Give the preparation type.
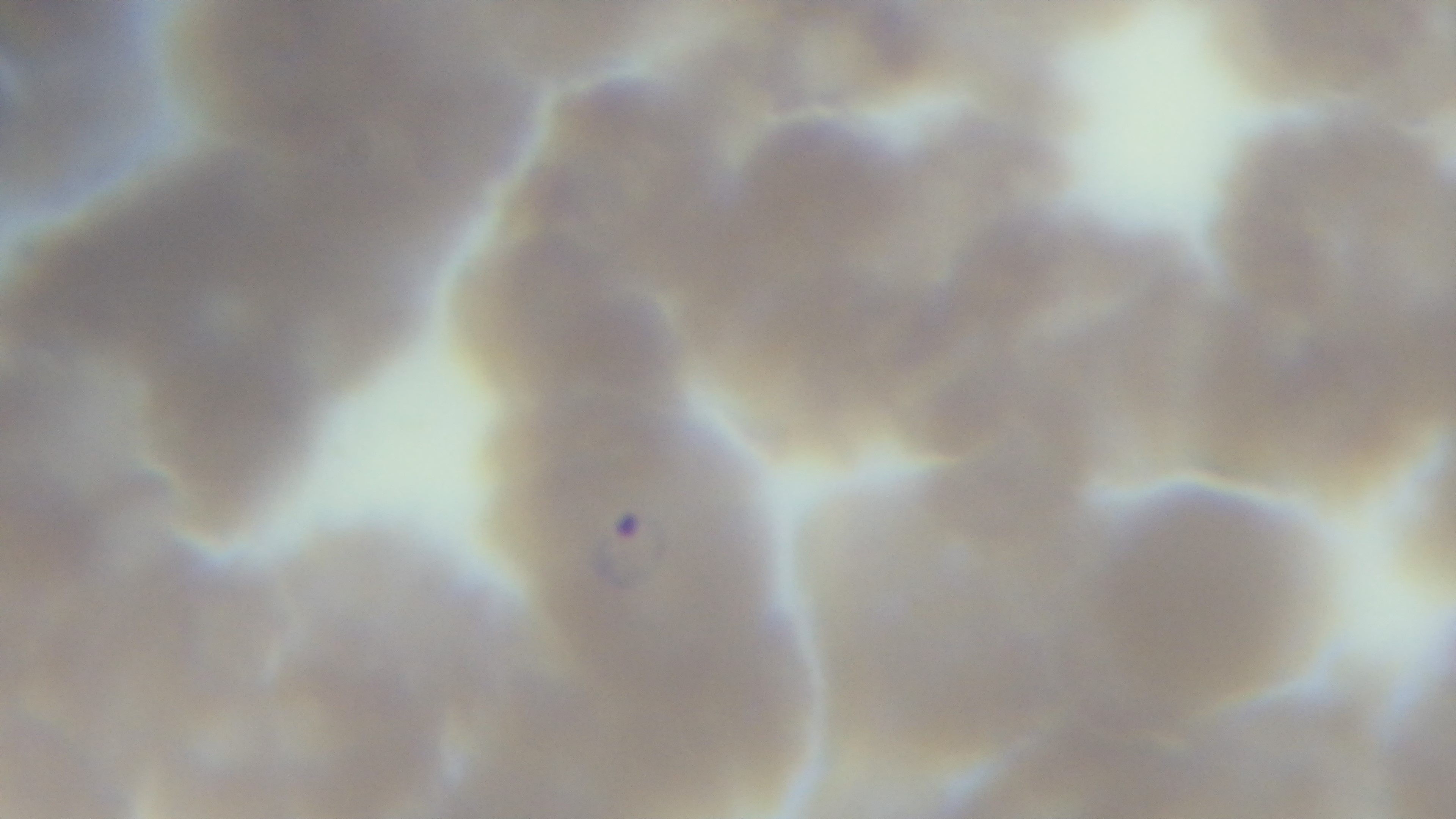

A thin smear.

stain: Giemsa
field_of_view: single
modality: light microscopy
objective: 100x oil immersion
malaria_status: infected
capture: mounted 4K digital camera